State which parasite is depicted.
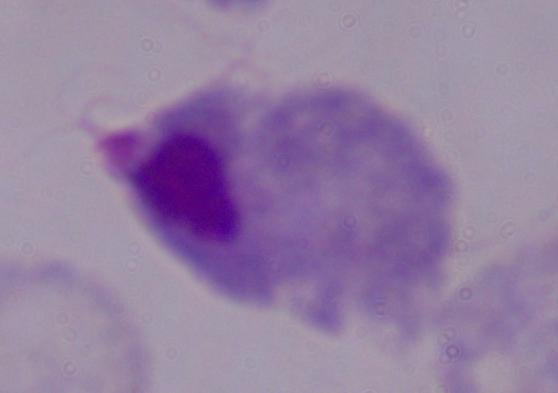

This is a trichomonad.

Summary:
  - Magnification: 1000x
  - Modality: micrograph